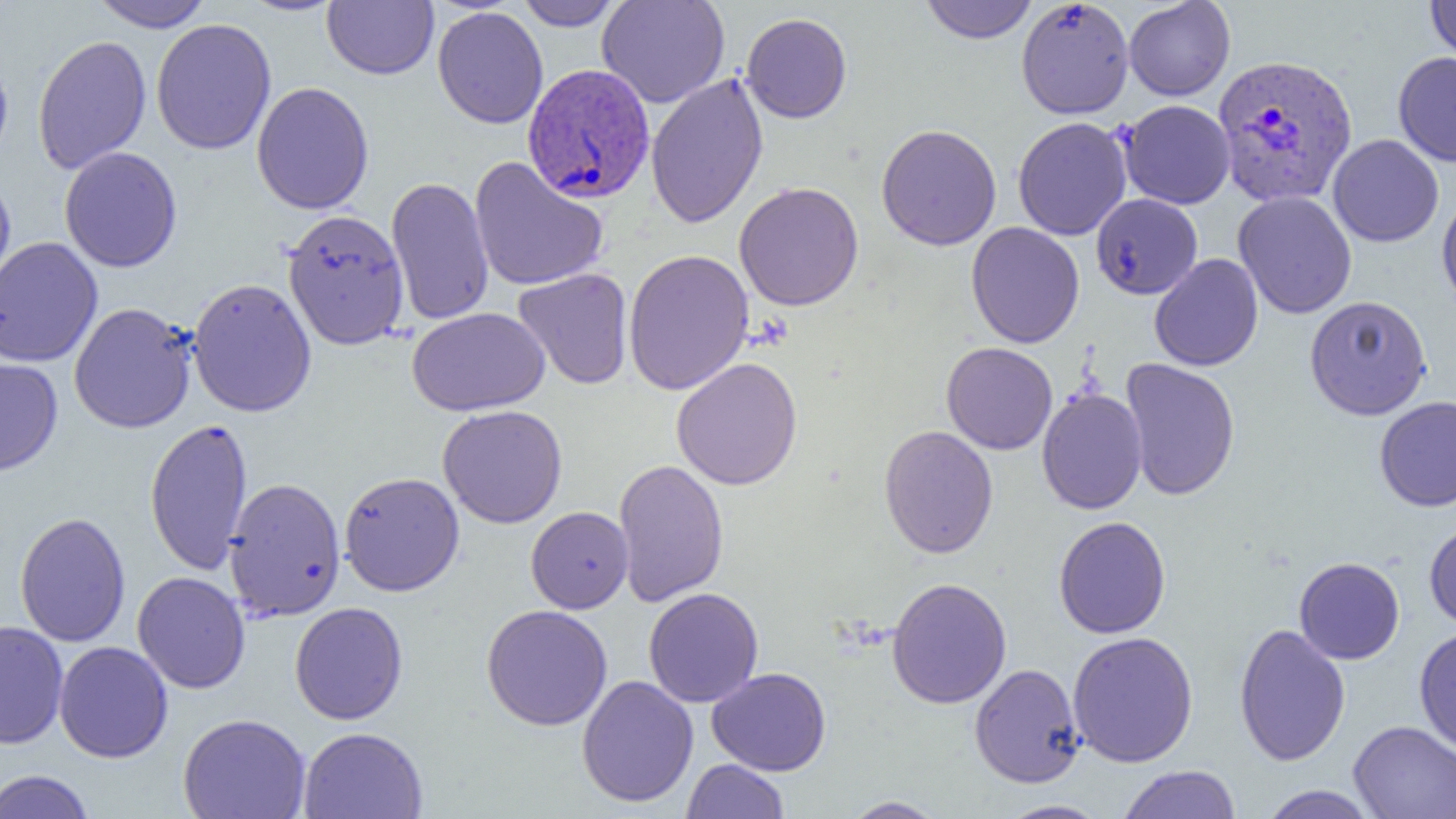

Summary:
  - Coordinate format: approximate bounding boxes as (x1,y1)-(x2,y2) corner pairs in pixels
  - Uninfected red blood cell locations: (89,0)-(213,32), (238,0)-(345,16), (515,0)-(624,31), (596,0)-(730,109), (920,0)-(1038,44), (1017,0)-(1134,117), (1425,0)-(1456,66), (322,1)-(438,80), (1123,1)-(1235,101), (432,6)-(548,129), (741,13)-(852,123), (151,19)-(277,155), (32,35)-(152,173), (1393,52)-(1456,167), (0,53)-(13,169), (646,71)-(768,229), (251,81)-(374,215), (1119,100)-(1235,209), (1013,116)-(1131,241), (876,124)-(1002,251), (1328,134)-(1444,247), (59,147)-(182,273), (469,157)-(609,292), (0,175)-(16,299), (386,176)-(494,325), (734,181)-(864,311), (1233,191)-(1357,319), (1091,193)-(1203,299), (1437,194)-(1456,313), (282,209)-(411,351), (966,222)-(1084,349), (0,236)-(103,368), (623,249)-(755,395), (1149,253)-(1263,371), (513,268)-(633,389), (187,278)-(317,418), (1304,295)-(1432,420), (68,302)-(198,433), (407,307)-(550,416), (941,341)-(1058,455), (0,357)-(63,477), (671,357)-(803,490), (1120,357)-(1240,501), (1036,388)-(1148,514), (1375,395)-(1456,512), (437,404)-(568,528), (145,417)-(253,576), (878,425)-(998,558), (613,457)-(729,608), (339,471)-(465,597), (224,477)-(346,621), (526,506)-(633,613), (14,511)-(131,647), (1053,516)-(1171,638), (1424,520)-(1456,632), (1294,557)-(1405,664), (132,571)-(250,694), (886,577)-(1012,709), (643,587)-(764,707), (290,602)-(408,725), (481,604)-(613,730), (1,620)-(68,749), (1233,623)-(1351,767), (1414,626)-(1456,755), (1067,630)-(1199,767), (54,641)-(173,763), (969,663)-(1085,788), (707,667)-(831,776), (576,675)-(698,807), (178,713)-(311,819), (1348,720)-(1456,819), (298,727)-(428,818), (681,759)-(790,818), (1117,765)-(1241,819), (0,770)-(96,819), (1258,785)-(1380,818), (840,796)-(948,818), (997,800)-(1110,818)
  - Plasmodium vivax-infected red blood cell locations: (1213,54)-(1358,208), (522,63)-(655,204)
  - Slide-level diagnosis: Plasmodium vivax
  - Magnification: 1000x
  - Image size: 1456×819 pixels
  - Preparation: thin blood film
  - Field of view: one of a larger specimen
  - Modality: optical microscopy